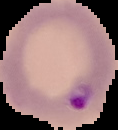

Summary:
  - Preparation: thin blood smear
  - Result: malaria parasites identified
  - Image size: 118×130 pixels
  - Image type: segmented cell region on a black background